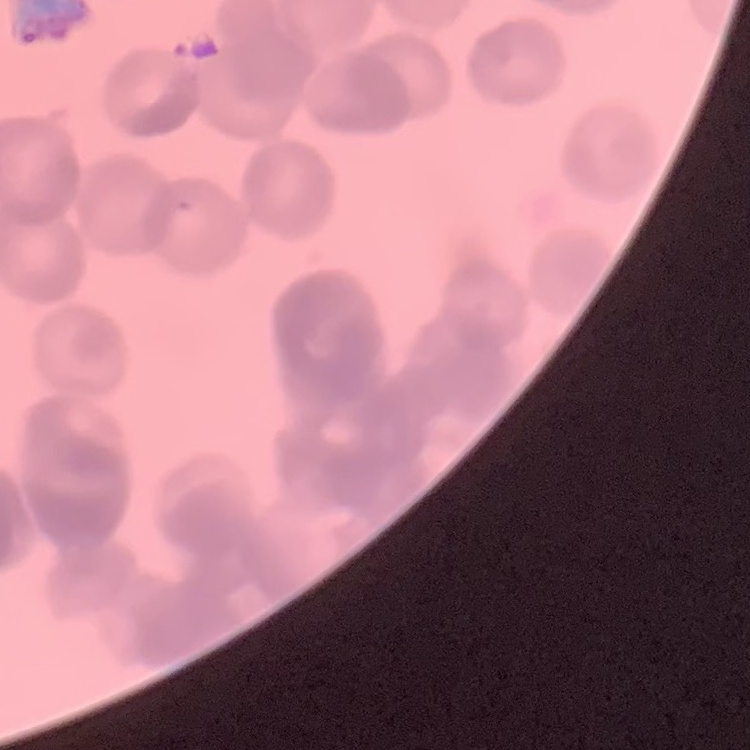 The erythrocytes exhibit rouleaux formation. Field's or Giemsa stain. Thin peripheral smear. One tile cut from a larger photomicrograph.